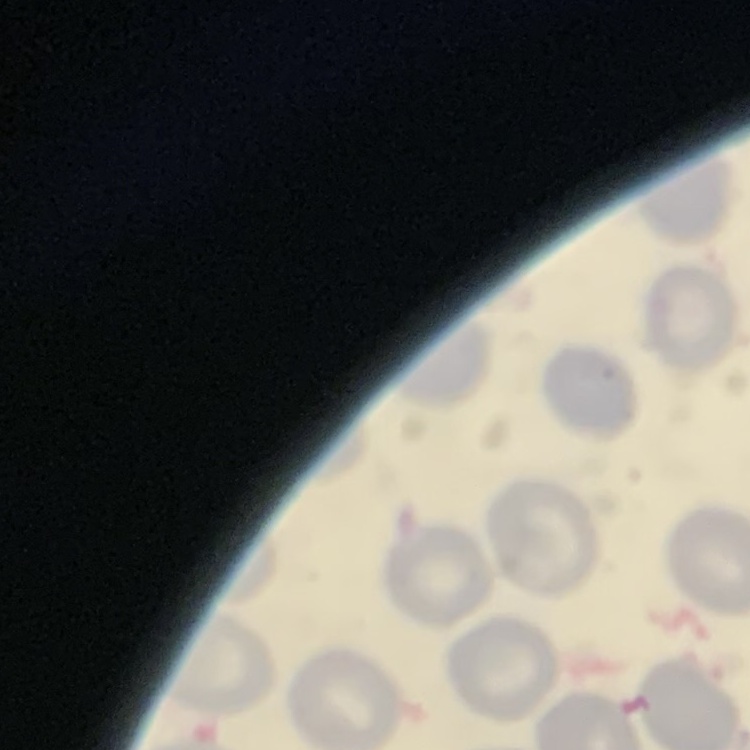
Summary:
  - Erythrocyte morphology: no rouleaux formation
  - Stain: Field's or Giemsa
  - Image type: one tile cut from a larger photomicrograph
  - Preparation: thin blood film